Name the blood parasite species.
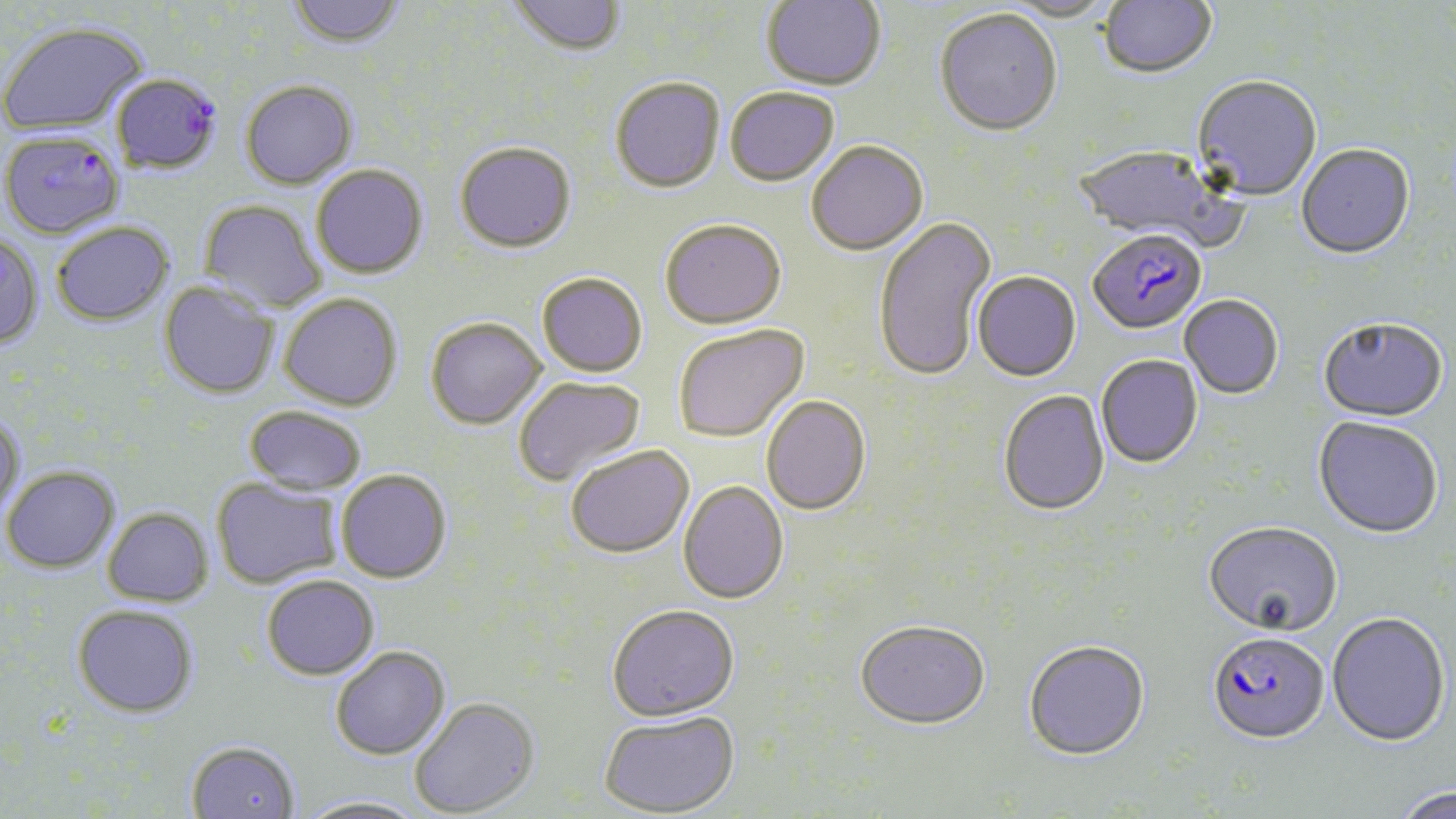

Plasmodium falciparum.

Summary:
  - Coordinate format: approximate bounding boxes as (x1,y1)-(x2,y2) corner pairs in pixels
  - Plasmodium falciparum-infected red blood cell locations: (1,132)-(124,240), (1088,231)-(1207,336), (1207,630)-(1330,742)
  - Uninfected red blood cell locations: (286,0)-(406,48), (506,0)-(627,56), (761,0)-(886,92), (1000,0)-(1118,24), (1099,0)-(1219,81), (934,11)-(1062,139), (0,21)-(148,135), (110,73)-(223,173), (610,76)-(725,192), (1192,78)-(1321,203), (240,79)-(357,189), (725,88)-(839,188), (454,140)-(577,252), (807,142)-(928,257), (1073,146)-(1233,252), (1296,146)-(1415,261), (311,164)-(428,278), (199,199)-(327,312), (873,216)-(996,382), (660,220)-(786,330), (51,222)-(174,325), (0,235)-(44,349), (536,272)-(647,377), (972,272)-(1080,382), (159,281)-(279,399), (279,292)-(403,411), (1180,296)-(1284,400), (425,317)-(546,429), (1318,319)-(1449,425), (673,324)-(809,443), (1096,355)-(1203,468), (513,375)-(646,488), (999,389)-(1110,516), (761,396)-(871,516), (244,406)-(367,494), (0,414)-(26,520), (1313,418)-(1443,540), (565,444)-(694,558), (1,466)-(120,573), (336,469)-(451,583), (211,478)-(343,588), (678,480)-(788,604), (103,507)-(214,606), (1203,521)-(1342,637), (262,575)-(379,680), (72,604)-(198,717), (606,604)-(740,720), (1327,612)-(1451,745), (854,619)-(990,731), (1023,639)-(1150,760), (330,645)-(450,760), (409,696)-(539,817), (599,710)-(740,816), (186,741)-(300,819), (1390,787)-(1456,819), (296,795)-(428,818)
  - Field of view: one of a larger specimen
  - Modality: light microscopy
  - Preparation: thin blood film
  - Stain: May-Grünwald-Giemsa
  - Image size: 1456×819 pixels
  - Magnification: 1000x